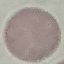

Result: no malaria parasites detected. Automatically extracted cell patch, resized to 64 × 64 pixels. Acquired by smartphone through the microscope eyepiece. Giemsa stain. Thin smear of blood.